Locate every blood parasite and identify its species.
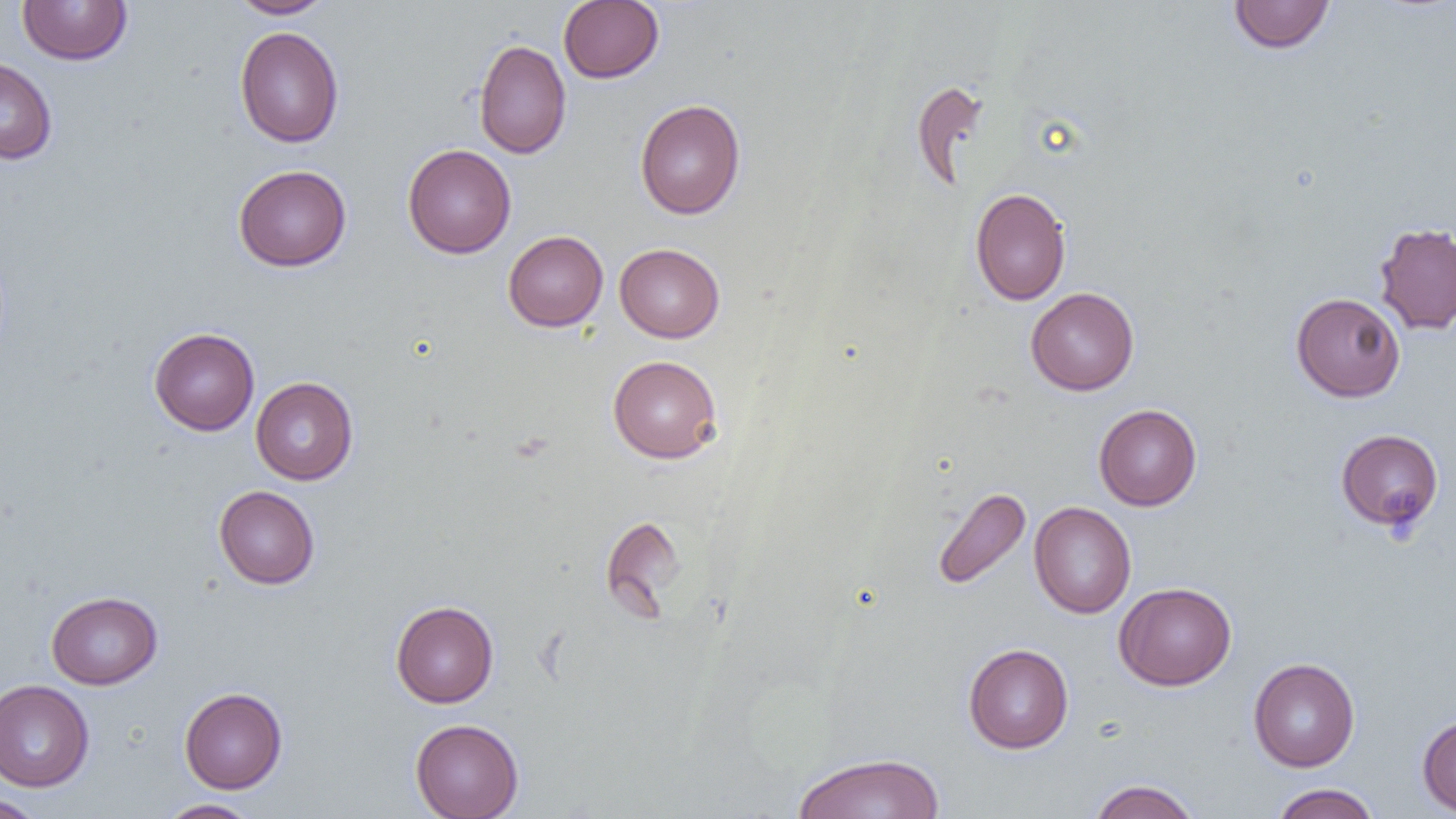
No blood parasites observed.

Summary:
  - Coordinate format: approximate bounding boxes as named x1/y1/x2/y2 corners in pixels
  - Uninfected red blood cell locations: (x1=17, y1=0, x2=133, y2=65), (x1=228, y1=0, x2=335, y2=19), (x1=1228, y1=0, x2=1335, y2=54), (x1=558, y1=1, x2=664, y2=83), (x1=234, y1=26, x2=344, y2=148), (x1=474, y1=39, x2=572, y2=159), (x1=0, y1=57, x2=58, y2=164), (x1=910, y1=81, x2=990, y2=192), (x1=634, y1=99, x2=746, y2=219), (x1=403, y1=144, x2=516, y2=258), (x1=233, y1=164, x2=352, y2=272), (x1=970, y1=187, x2=1071, y2=305), (x1=1374, y1=222, x2=1456, y2=335), (x1=503, y1=230, x2=608, y2=331), (x1=615, y1=243, x2=725, y2=342), (x1=1026, y1=287, x2=1139, y2=396), (x1=1291, y1=293, x2=1405, y2=402), (x1=149, y1=327, x2=260, y2=435), (x1=608, y1=355, x2=723, y2=464), (x1=251, y1=377, x2=358, y2=485), (x1=1094, y1=404, x2=1202, y2=510), (x1=1335, y1=428, x2=1444, y2=532), (x1=213, y1=485, x2=320, y2=589), (x1=932, y1=486, x2=1031, y2=591), (x1=1029, y1=501, x2=1136, y2=618), (x1=600, y1=514, x2=687, y2=619), (x1=1114, y1=582, x2=1237, y2=690), (x1=46, y1=591, x2=162, y2=689), (x1=390, y1=600, x2=499, y2=708), (x1=963, y1=643, x2=1074, y2=753), (x1=1248, y1=657, x2=1360, y2=772), (x1=0, y1=679, x2=94, y2=792), (x1=179, y1=687, x2=287, y2=793), (x1=1417, y1=713, x2=1456, y2=816), (x1=410, y1=718, x2=524, y2=819), (x1=792, y1=752, x2=946, y2=819), (x1=1087, y1=779, x2=1201, y2=819), (x1=1271, y1=783, x2=1381, y2=819), (x1=0, y1=795, x2=47, y2=818), (x1=156, y1=799, x2=260, y2=818)
  - Slide-level diagnosis: no evidence of blood parasites
  - Magnification: 1000x
  - Modality: optical microscopy
  - Image size: 1456×819 pixels
  - Field of view: one of a larger specimen
  - Preparation: thin blood smear